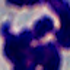
modality: photomicrograph
identification: leukocyte
magnification: 1000x